Classify this cell by malaria status.
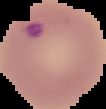

It is parasitized.

Summary:
  - Image size: 106×109 pixels
  - Preparation: thin blood film
  - Image type: segmented cell region on a black background